Describe the morphology of the erythrocytes.
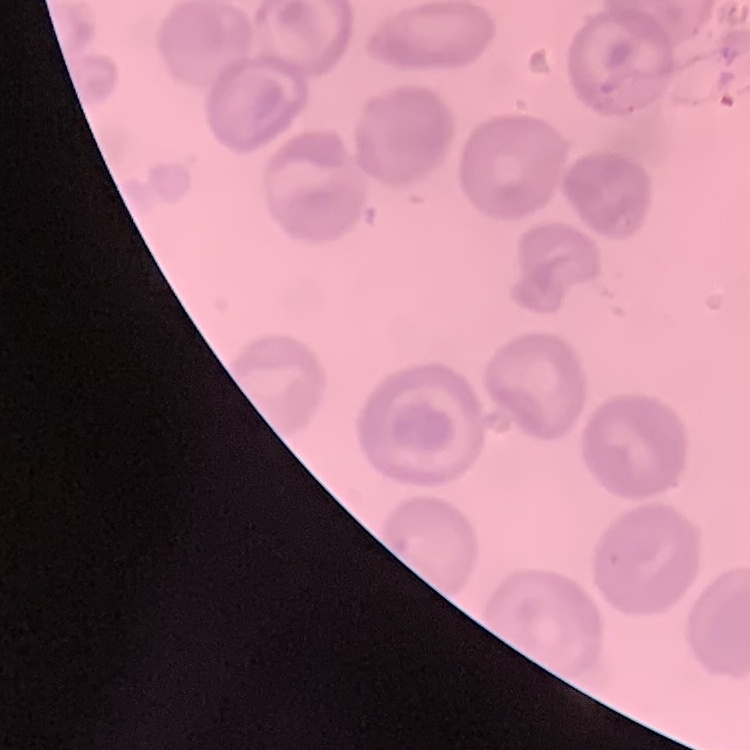

No rouleaux formation.

One tile cut from a larger photomicrograph. Thin blood smear. Stained with either Field's or Giemsa.